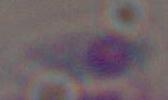

Photomicrograph. 1000x magnification. Toxoplasma gondii is seen.